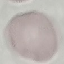

Malaria status: uninfected. Acquired by smartphone through the microscope eyepiece. Giemsa-stained preparation. Thin blood smear. Cell patch, automatically extracted from a larger field of view and resized to 64 × 64 pixels.